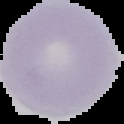 Malaria status: uninfected. From a thin blood film. Segmented cell region on a black background. Image is 124×124 pixels.